Assess this cell for malaria.
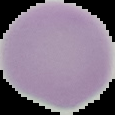
It is uninfected.

Cell region segmented out of the field of view; the surrounding area is masked to black. From a thin blood film. Image is 115×115 pixels.